Assess this cell for malaria.
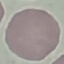

Uninfected.

Giemsa stain. Automatically extracted cell patch, resized to 64 × 64 pixels. Photographed with a smartphone camera at the microscope eyepiece. Thin blood smear.